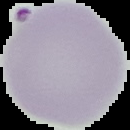 Cell region segmented out of the field of view; the surrounding area is masked to black. Image is 130×130 pixels. From a thin blood film. Result: Plasmodium parasites detected.